Name the parasite shown.
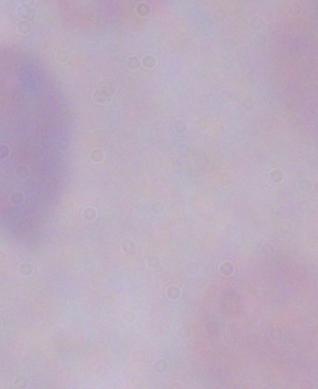

A trypanosome.

{
  "magnification": "1000x",
  "modality": "micrograph"
}